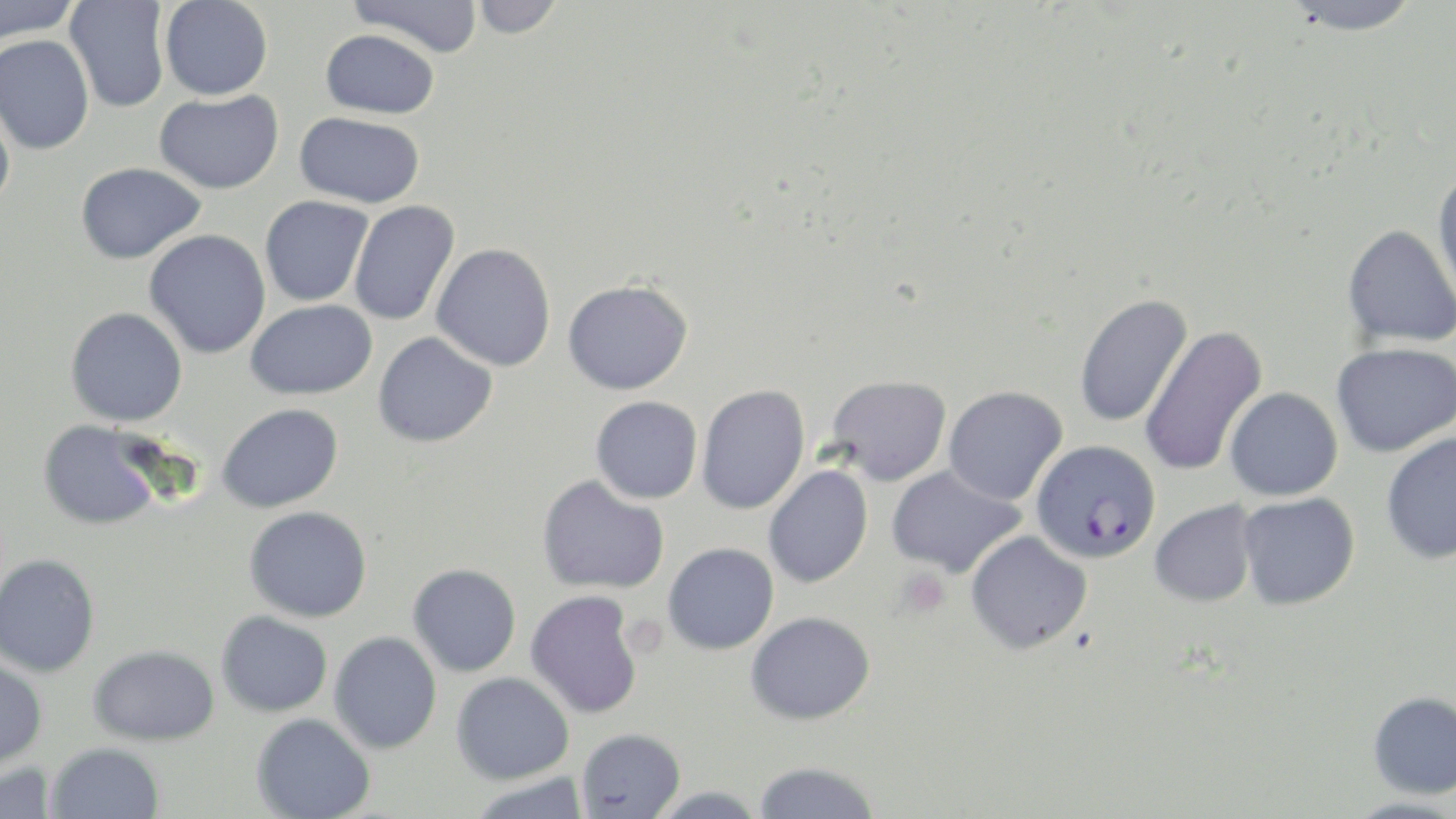
slide-level diagnosis = Plasmodium falciparum
modality = optical microscopy
preparation = thin blood smear
stain = May-Grünwald-Giemsa
Plasmodium falciparum-infected red blood cell locations = approximate bounding boxes as (x1,y1)-(x2,y2) corner pairs in pixels: (1032,440)-(1161,563)
magnification = 1000x
platelet locations = approximate bounding boxes as (x1,y1)-(x2,y2) corner pairs in pixels: (895,567)-(952,619), (630,616)-(670,659)
uninfected red blood cell locations = approximate bounding boxes as (x1,y1)-(x2,y2) corner pairs in pixels: (0,0)-(79,44), (348,0)-(483,58), (469,0)-(565,40), (1282,0)-(1425,35), (65,1)-(170,114), (160,1)-(273,100), (321,29)-(439,118), (0,33)-(94,155), (154,90)-(283,194), (0,91)-(16,213), (294,111)-(424,207), (76,162)-(205,264), (1432,168)-(1456,305), (260,195)-(373,306), (348,200)-(460,326), (1342,224)-(1456,348), (144,229)-(271,359), (431,243)-(556,371), (563,279)-(692,394), (1074,293)-(1193,428), (245,299)-(377,400), (65,307)-(187,427), (1139,325)-(1268,478), (373,331)-(497,448), (1331,342)-(1456,457), (826,375)-(952,486), (696,384)-(810,515), (943,386)-(1068,505), (1225,386)-(1343,500), (590,396)-(703,504), (216,403)-(344,513), (39,420)-(163,530), (1381,431)-(1456,564), (763,465)-(873,589), (886,465)-(1027,578), (537,475)-(670,595), (1238,492)-(1360,610), (1149,499)-(1258,608), (244,506)-(372,622), (965,531)-(1092,654), (663,543)-(779,655), (0,553)-(100,678), (408,563)-(521,677), (525,590)-(643,719), (216,611)-(333,717), (746,611)-(875,725), (329,631)-(442,754), (88,645)-(219,745), (0,659)-(47,771), (451,672)-(574,785), (1367,691)-(1456,798), (252,713)-(375,818), (577,728)-(685,818), (47,742)-(164,818), (752,761)-(880,819), (0,762)-(58,819), (466,773)-(593,819), (646,786)-(767,818), (1340,797)-(1456,819)
field of view = single
image size = 1456×819 pixels